Assess this cell for malaria.
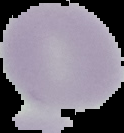
It is uninfected.

Summary:
  - Image size: 124×133 pixels
  - Image type: segmented cell region on a black background
  - Preparation: thin blood film